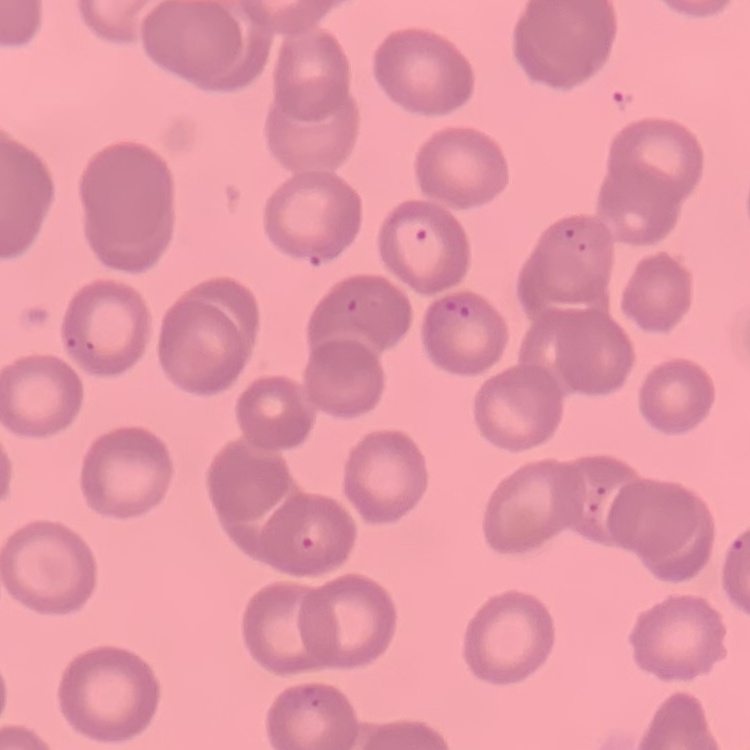
Summary:
  - Erythrocyte morphology: no rouleaux formation
  - Image type: one tile cut from a larger photomicrograph
  - Stain: Field's or Giemsa
  - Preparation: thin blood smear